Identify the parasite.
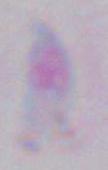

Toxoplasma gondii.

Summary:
  - Modality: micrograph
  - Magnification: 1000x